Assess this cell for malaria.
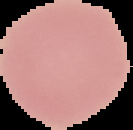

Uninfected.

Summary:
  - Image type: cell region segmented out of the field of view; surrounding area masked to black
  - Preparation: thin blood film
  - Image size: 133×130 pixels